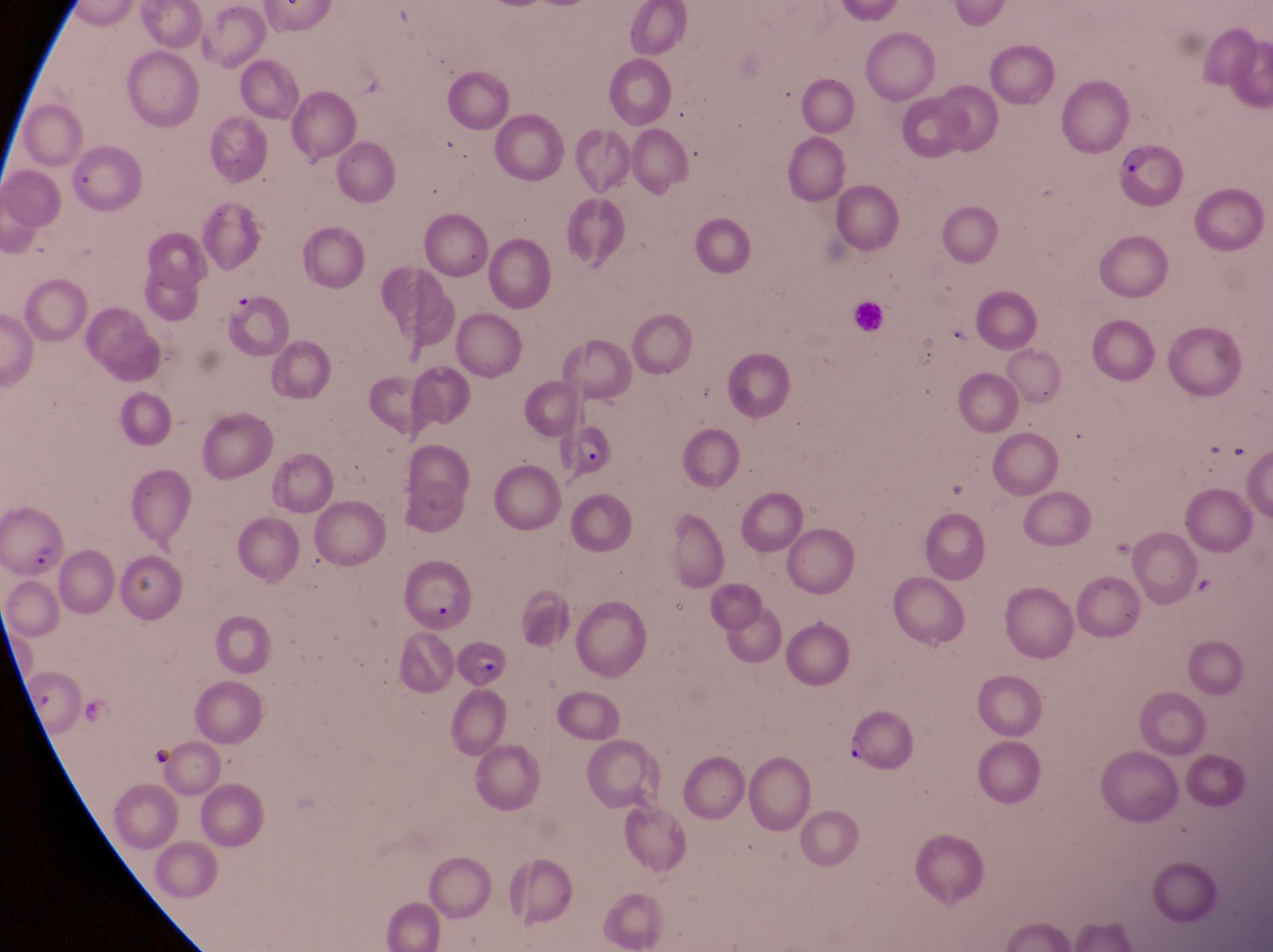
Approximate bounding boxes as {left, top, right, bottom} in pixels.
Summary:
  - Parasitised red blood cell locations: {1111, 142, 1185, 210}, {222, 287, 287, 359}, {556, 420, 616, 482}, {3, 500, 66, 583}, {405, 561, 475, 635}, {454, 634, 509, 689}
  - Artifact (platelet-like body, stain precipitate, or debris) locations: {1231, 435, 1258, 475}, {1195, 575, 1218, 600}
  - Leukocyte locations: {851, 295, 885, 333}
  - Preparation: thin blood film
  - Image size: 1273×952 pixels
  - Magnification: 1000x
  - Country: Uganda
  - Capture: smartphone photograph through the eyepiece of an Olympus CX-23 microscope
  - Field of view: single